State the blood parasite species.
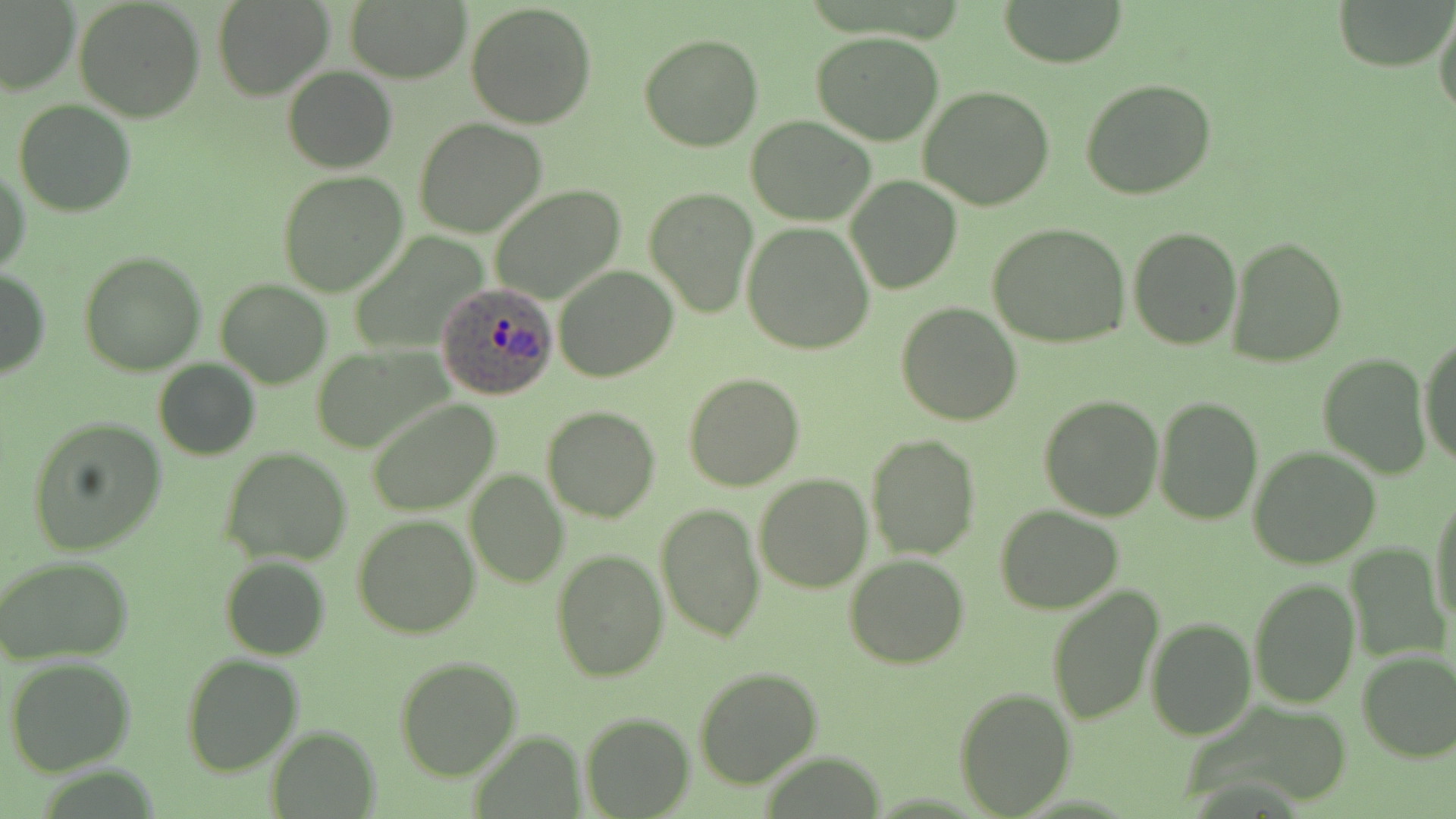
Plasmodium ovale.

preparation = thin blood film
field of view = one of a larger specimen
Plasmodium ovale-infected red blood cell locations = approximate bounding boxes as (x1, y1, x2, y2) in pixels: (437, 282, 557, 400)
magnification = 1000x
uninfected red blood cell locations = approximate bounding boxes as (x1, y1, x2, y2) in pixels: (73, 0, 204, 121), (214, 0, 334, 100), (998, 0, 1128, 69), (1335, 0, 1450, 72), (0, 1, 79, 96), (346, 1, 470, 83), (465, 3, 597, 130), (1433, 5, 1456, 120), (811, 31, 947, 146), (639, 32, 763, 151), (283, 66, 397, 172), (1079, 78, 1217, 199), (919, 86, 1057, 210), (14, 100, 137, 217), (747, 115, 876, 224), (415, 119, 548, 238), (1, 163, 30, 277), (279, 172, 408, 297), (847, 177, 962, 294), (489, 185, 625, 302), (645, 187, 757, 317), (741, 222, 875, 354), (987, 222, 1130, 348), (1128, 226, 1242, 350), (1226, 235, 1349, 368), (78, 251, 205, 375), (553, 264, 678, 382), (0, 268, 49, 379), (215, 278, 334, 387), (897, 301, 1021, 425), (1419, 332, 1456, 469), (312, 344, 453, 451), (1317, 353, 1431, 477), (153, 359, 260, 461), (683, 372, 804, 491), (1039, 394, 1164, 520), (1153, 395, 1262, 523), (366, 398, 500, 515), (542, 406, 661, 523), (26, 416, 169, 557), (865, 433, 980, 559), (1249, 446, 1382, 568), (219, 447, 353, 565), (464, 471, 568, 588), (754, 472, 872, 592), (1430, 488, 1456, 629), (655, 504, 765, 642), (995, 504, 1124, 615), (352, 514, 479, 639), (1345, 543, 1448, 666), (551, 549, 668, 681), (0, 555, 134, 665), (220, 555, 329, 660), (844, 555, 969, 668), (1249, 577, 1359, 707), (1047, 586, 1163, 726), (1146, 614, 1256, 739), (1357, 649, 1456, 763), (181, 654, 304, 775), (393, 655, 521, 780), (6, 656, 137, 775), (692, 666, 823, 788), (954, 685, 1078, 817), (581, 713, 694, 817), (265, 726, 378, 816)
stain = May-Grünwald-Giemsa
modality = optical microscopy
image size = 1456×819 pixels